Describe the morphology of the erythrocytes.
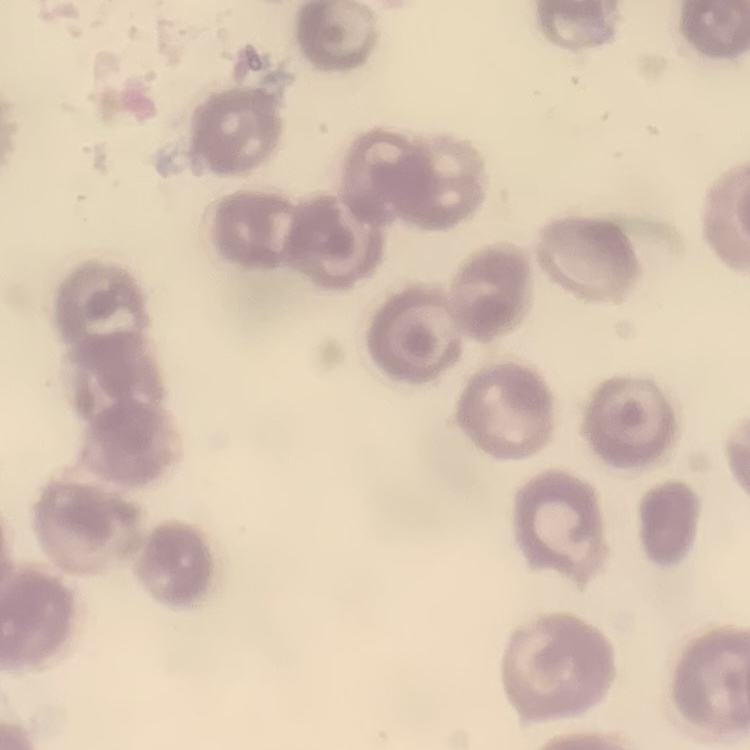
They show no rouleaux formation.

Summary:
  - Preparation: thin peripheral smear
  - Image type: square crop of a larger photomicrograph
  - Stain: Field's or Giemsa